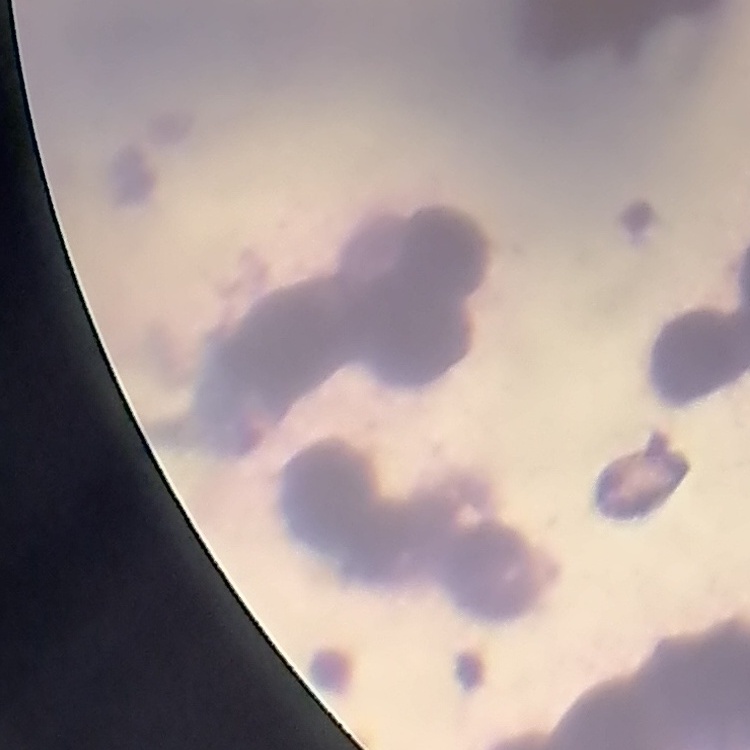

The erythrocytes exhibit rouleaux formation. Thin blood film. Field's or Giemsa stain. One tile cut from a larger photomicrograph.